Assess this cell for malaria.
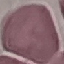
Uninfected.

Giemsa stain. Thin blood film. Photographed with a smartphone camera at the microscope eyepiece. Cell patch, automatically extracted from a larger field of view and resized to 64 × 64 pixels.